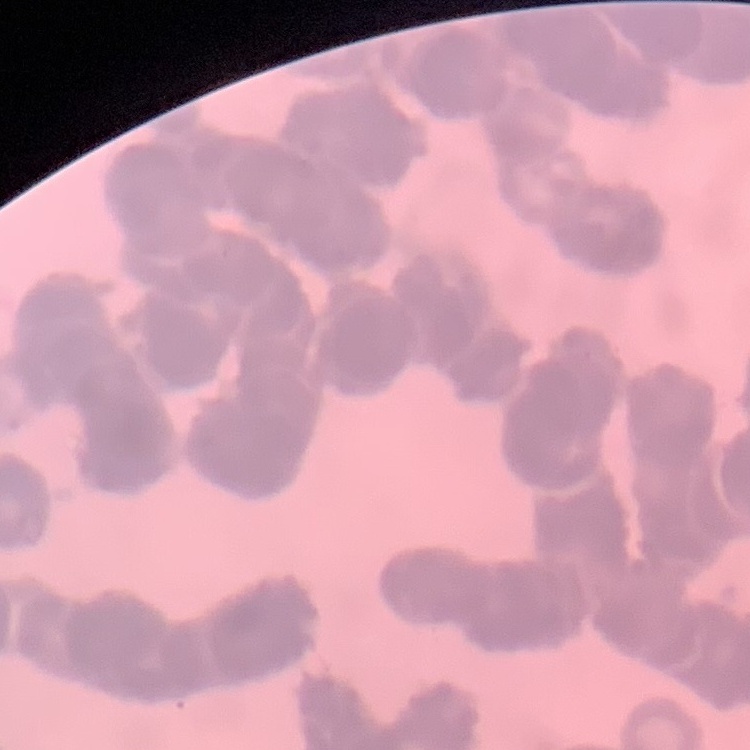
Summary:
  - Red blood cell morphology: rouleaux formation
  - Preparation: thin peripheral smear
  - Image type: one tile cut from a larger photomicrograph
  - Stain: Field's or Giemsa